Outline each blood parasite and name the species.
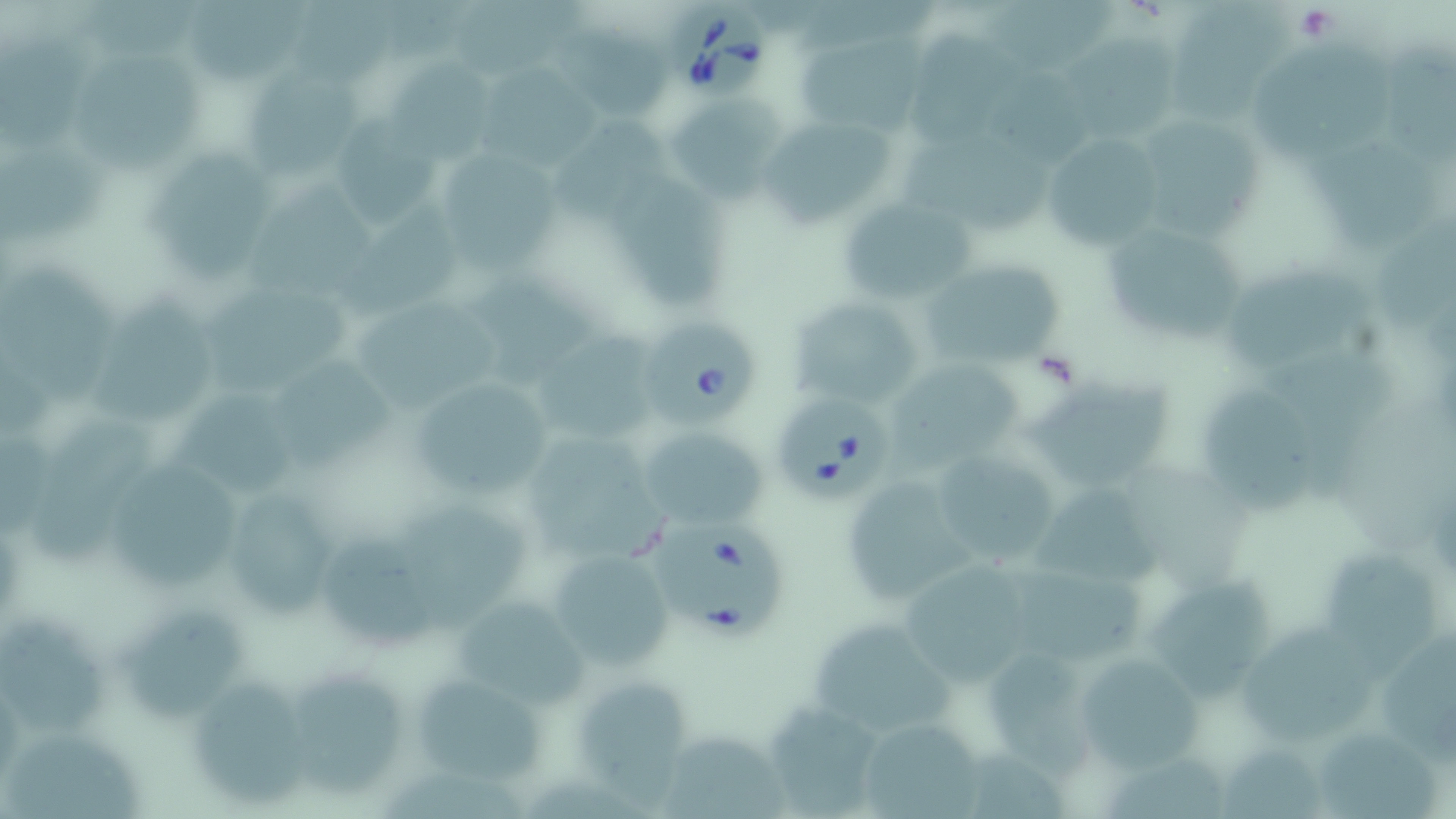
Approximate bounding boxes as (x1, y1, x2, y2) in pixels.
Babesia divergens-infected red blood cells: (666, 4, 772, 105), (643, 322, 757, 432), (780, 399, 899, 498), (648, 519, 795, 640).
No Plasmodium falciparum, Plasmodium ovale, Plasmodium malariae, Plasmodium vivax, or Trypanosoma brucei observed.

slide-level diagnosis = Babesia divergens
platelet locations = approximate bounding boxes as (x1, y1, x2, y2) in pixels: (1290, 5, 1339, 40)
field of view = single
uninfected red blood cell locations = approximate bounding boxes as (x1, y1, x2, y2) in pixels: (82, 0, 203, 62), (455, 0, 584, 74), (1170, 0, 1296, 122), (191, 1, 304, 82), (291, 1, 400, 85), (985, 4, 1122, 69), (906, 27, 1019, 145), (557, 28, 680, 121), (1383, 30, 1456, 166), (797, 31, 924, 134), (1064, 32, 1181, 138), (1, 38, 90, 150), (1253, 44, 1396, 161), (77, 52, 206, 175), (392, 57, 500, 165), (243, 65, 365, 182), (481, 66, 607, 172), (674, 98, 786, 204), (332, 110, 440, 225), (765, 118, 897, 227), (1152, 119, 1265, 242), (554, 120, 670, 226), (1042, 131, 1166, 254), (904, 133, 1053, 234), (1307, 140, 1438, 254), (1, 150, 108, 249), (442, 152, 559, 279), (149, 154, 279, 280), (613, 160, 732, 308), (256, 177, 378, 299), (837, 195, 972, 305), (1369, 209, 1456, 333), (1114, 234, 1247, 340), (2, 263, 110, 406), (922, 264, 1064, 372), (1224, 267, 1380, 367), (470, 271, 589, 388), (204, 286, 352, 395), (85, 290, 220, 425), (789, 291, 928, 411), (357, 302, 501, 414), (540, 329, 658, 438), (1278, 353, 1393, 498), (273, 359, 396, 470), (890, 364, 1026, 469), (1024, 374, 1175, 495), (405, 376, 560, 502), (1206, 387, 1324, 518), (171, 388, 294, 497), (30, 413, 155, 570), (638, 426, 768, 529), (531, 434, 669, 557), (930, 449, 1065, 568), (112, 459, 239, 590), (839, 475, 973, 606), (217, 484, 342, 622), (1028, 485, 1168, 586), (401, 499, 528, 627), (322, 534, 439, 651), (543, 546, 675, 672), (1324, 546, 1435, 687), (899, 558, 1039, 682), (1013, 563, 1147, 663), (1146, 578, 1274, 704), (450, 597, 596, 709), (122, 602, 245, 721), (2, 607, 103, 738), (1237, 620, 1383, 743), (1386, 624, 1456, 770), (814, 625, 961, 730), (1075, 650, 1205, 772), (985, 652, 1100, 791), (294, 665, 401, 797), (408, 669, 551, 787), (191, 672, 311, 805), (576, 679, 685, 809), (761, 705, 884, 813), (855, 715, 987, 818), (1322, 727, 1441, 819), (659, 730, 788, 819), (1, 731, 144, 819), (1222, 745, 1327, 819), (1110, 754, 1223, 816)
modality = optical microscopy
preparation = thin blood smear
image size = 1456×819 pixels
magnification = 1000x
stain = May-Grünwald-Giemsa